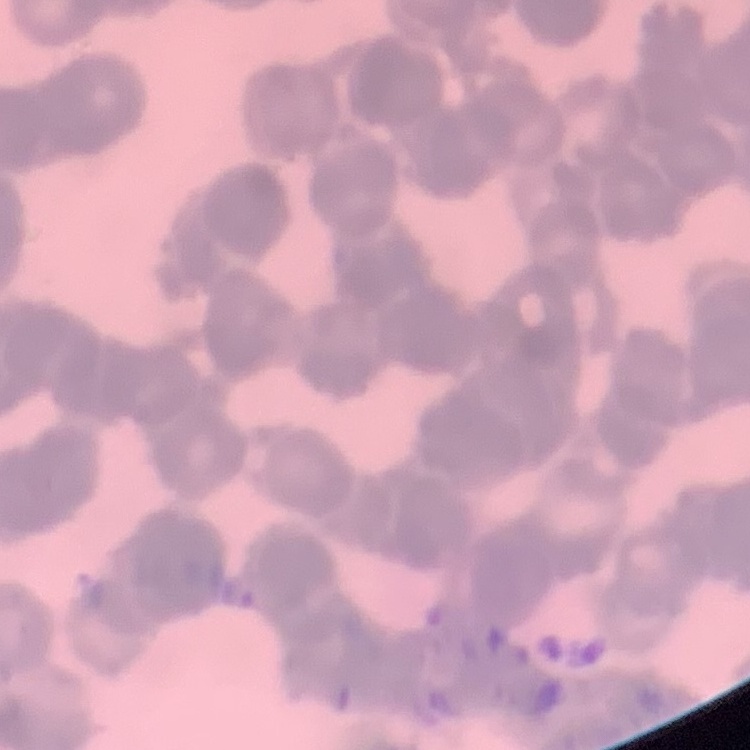
erythrocyte morphology = rouleaux formation
image type = one tile cut from a larger photomicrograph
preparation = thin blood film
stain = Field's or Giemsa